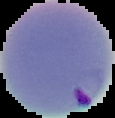

Summary:
  - Image type: segmented cell region on a black background
  - Malaria status: parasitized
  - Image size: 115×118 pixels
  - Preparation: thin blood smear